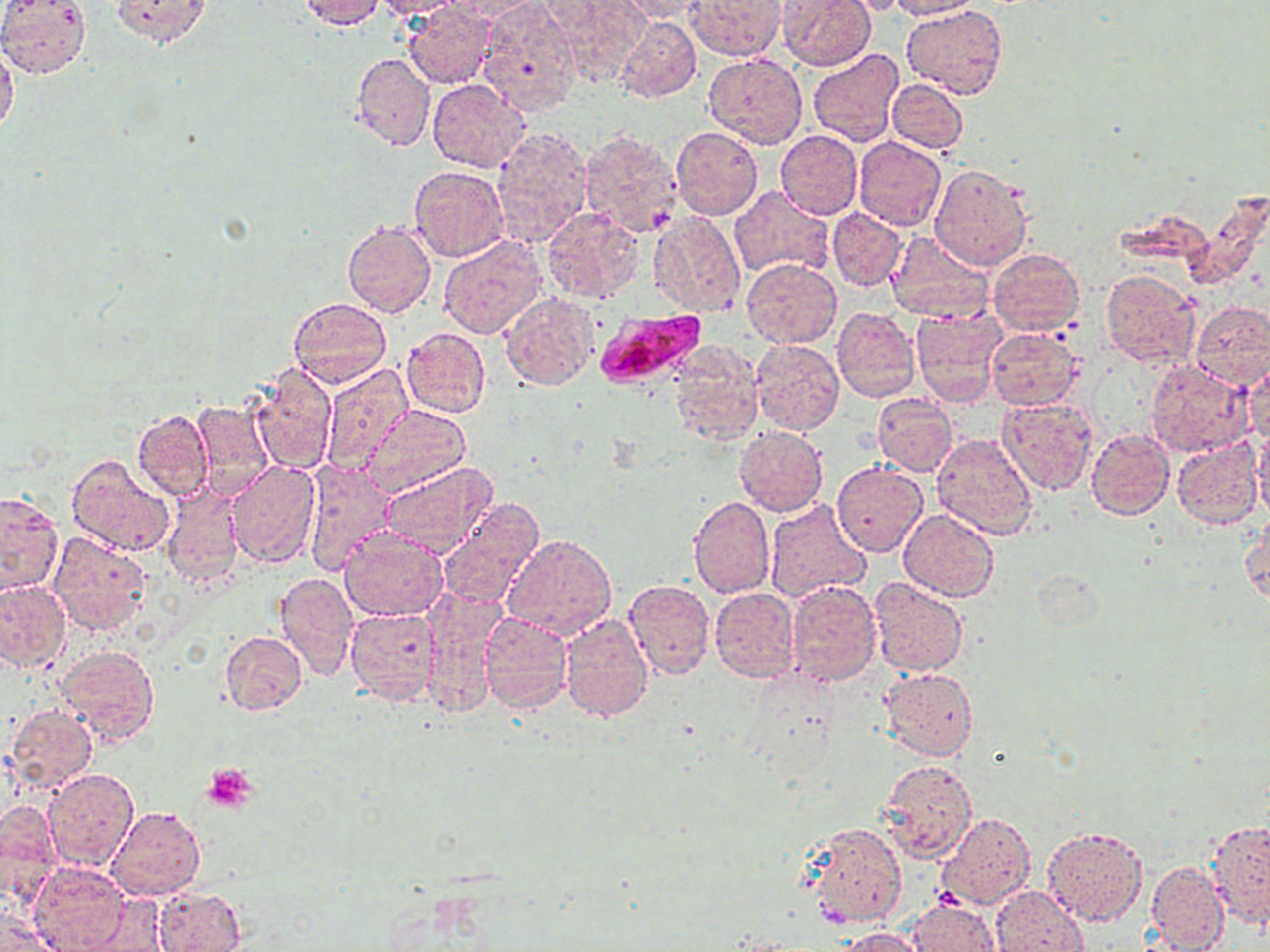
Summary:
  - Coordinate format: approximate bounding boxes as [x1, y1, x2, y2] in pixels
  - Plasmodium falciparum-infected red blood cell locations: [596, 312, 708, 386]
  - Platelet locations: [202, 763, 257, 813]
  - Uninfected red blood cell locations: [0, 0, 90, 77], [108, 0, 212, 45], [296, 0, 385, 29], [371, 0, 465, 19], [449, 0, 548, 20], [687, 0, 785, 60], [778, 0, 874, 71], [840, 0, 916, 15], [886, 0, 979, 20], [475, 1, 582, 116], [550, 1, 649, 83], [618, 1, 710, 21], [402, 3, 496, 89], [902, 4, 1006, 100], [614, 17, 701, 103], [0, 44, 20, 136], [807, 49, 904, 146], [704, 51, 808, 148], [350, 53, 434, 151], [426, 79, 532, 172], [888, 79, 968, 152], [490, 127, 592, 248], [671, 127, 762, 220], [578, 129, 683, 239], [775, 130, 862, 218], [854, 137, 946, 232], [929, 164, 1031, 271], [408, 166, 507, 262], [729, 186, 835, 281], [541, 207, 644, 303], [828, 208, 906, 290], [647, 210, 744, 318], [342, 219, 435, 317], [885, 230, 996, 322], [437, 234, 546, 339], [988, 248, 1085, 336], [742, 260, 841, 347], [1099, 269, 1200, 368], [501, 293, 597, 390], [288, 297, 392, 389], [1190, 301, 1270, 390], [911, 306, 1006, 408], [832, 307, 921, 402], [400, 326, 491, 418], [985, 327, 1084, 410], [751, 339, 844, 436], [668, 346, 762, 447], [1147, 360, 1252, 457], [1245, 360, 1270, 447], [250, 364, 337, 473], [318, 365, 415, 475], [872, 394, 956, 476], [194, 398, 275, 500], [997, 398, 1099, 496], [364, 404, 471, 496], [130, 408, 215, 502], [733, 425, 829, 517], [1252, 427, 1270, 523], [1085, 428, 1174, 520], [931, 433, 1038, 540], [1172, 436, 1263, 529], [65, 453, 175, 557], [300, 459, 398, 578], [225, 461, 322, 567], [378, 461, 497, 556], [832, 463, 928, 558], [161, 486, 242, 586], [0, 491, 62, 594], [689, 496, 775, 598], [437, 498, 544, 608], [765, 499, 871, 604], [898, 508, 998, 600], [1242, 515, 1270, 606], [338, 530, 446, 620], [47, 533, 152, 636], [502, 533, 616, 641], [1031, 568, 1103, 633], [273, 571, 358, 681], [0, 578, 71, 674], [785, 578, 881, 685], [868, 578, 966, 677], [623, 579, 716, 679], [709, 588, 799, 683], [420, 591, 502, 719], [344, 606, 442, 703], [478, 612, 572, 713], [559, 614, 653, 722], [220, 630, 307, 715], [54, 643, 160, 745], [880, 668, 978, 760], [5, 703, 98, 794], [881, 760, 977, 863], [44, 769, 139, 871], [0, 800, 61, 902], [107, 807, 204, 900], [934, 812, 1036, 910], [1207, 819, 1270, 927], [806, 821, 907, 930], [1043, 826, 1147, 925], [29, 861, 131, 951], [1147, 861, 1229, 951], [152, 886, 246, 952], [991, 886, 1085, 951], [73, 897, 172, 952], [909, 897, 997, 952], [0, 910, 57, 951], [837, 926, 927, 951]
  - Slide-level diagnosis: Plasmodium falciparum
  - Image size: 1270×952 pixels
  - Field of view: one of a larger specimen
  - Preparation: thin blood smear
  - Modality: light microscopy
  - Stain: May-Grünwald-Giemsa
  - Magnification: 1000x